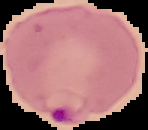 Malaria status: parasitized. Segmented cell region on a black background. Image is 148×130 pixels. From a thin blood film.